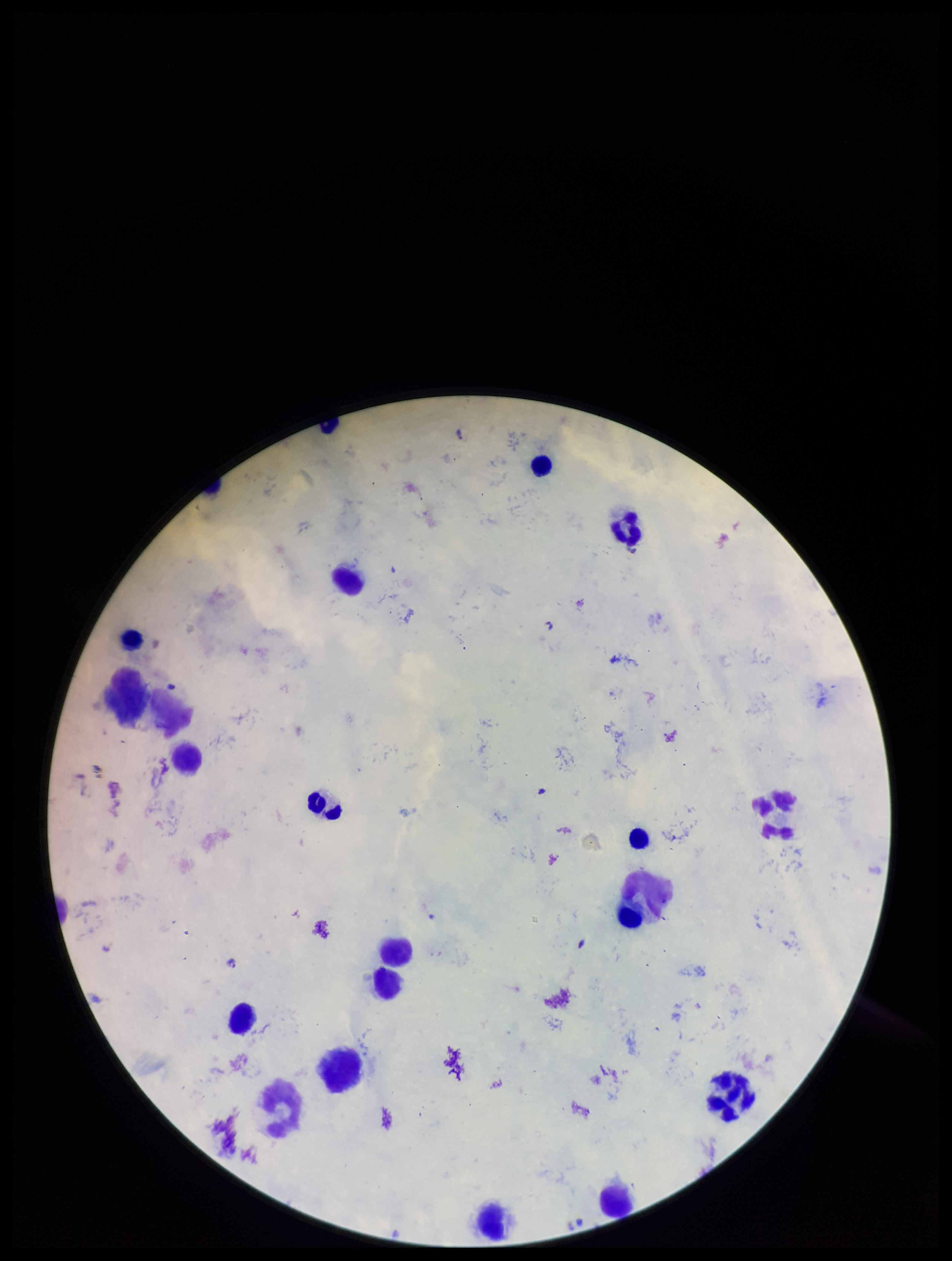

Summary:
  - Parasite count: 2
  - Field of view: single
  - Image size: 952×1261 pixels
  - Patient malaria status: positive
  - Capture: smartphone photograph through the microscope eyepiece
  - Species reported for this patient: Plasmodium falciparum
  - Leukocyte count: 15
  - Plasmodium parasites: seen
  - Stain: Giemsa
  - Preparation: thick